Describe the morphology of the red blood cells.
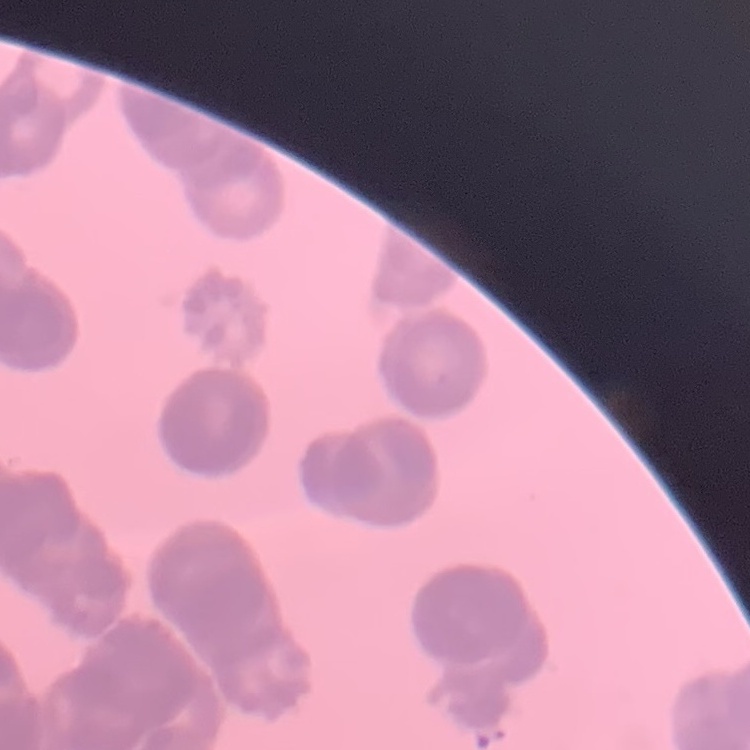
Rouleaux formation.

image_type: square crop of a larger photomicrograph
preparation: thin blood smear
stain: Field's or Giemsa